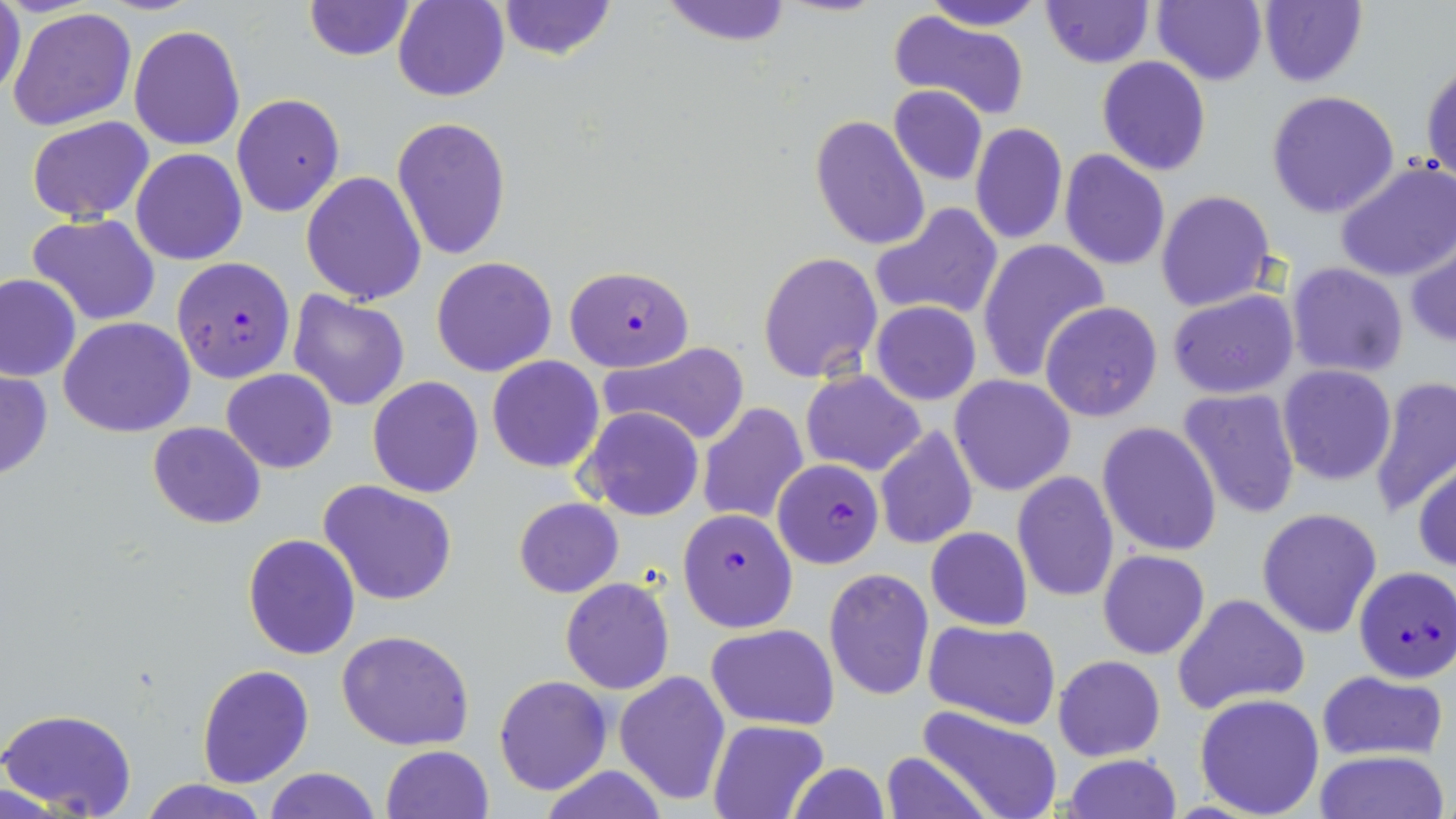

Approximate bounding boxes as (x1,y1)-(x2,y2) corner pairs in pixels. Uninfected red blood cell locations: (0,0)-(27,103), (303,0)-(416,60), (393,0)-(508,102), (492,0)-(619,63), (658,0)-(796,46), (920,0)-(1046,30), (1152,0)-(1267,85), (1260,0)-(1368,87), (1041,1)-(1155,68), (9,7)-(137,132), (888,11)-(1028,121), (130,24)-(246,151), (1421,54)-(1455,187), (1097,56)-(1211,176), (888,85)-(989,186), (1266,90)-(1400,218), (230,94)-(345,216), (809,114)-(929,252), (27,115)-(155,224), (392,116)-(512,261), (969,122)-(1068,246), (131,149)-(247,264), (1060,150)-(1170,272), (1335,161)-(1456,282), (300,171)-(426,305), (1155,190)-(1276,312), (871,203)-(1003,320), (29,212)-(161,325), (976,238)-(1110,384), (1406,243)-(1456,347), (758,251)-(883,384), (431,255)-(558,377), (1286,262)-(1408,379), (0,273)-(81,381), (1167,289)-(1299,400), (287,290)-(411,411), (871,301)-(981,405), (1040,301)-(1163,421), (59,316)-(196,438), (598,341)-(749,445), (487,356)-(606,472), (1278,365)-(1397,485), (0,367)-(52,483), (222,369)-(337,474), (800,370)-(926,476), (949,375)-(1077,496), (367,376)-(484,498), (1368,377)-(1456,522), (1177,387)-(1300,522), (697,402)-(809,525), (583,407)-(703,522), (147,421)-(266,529), (1097,422)-(1222,556), (874,425)-(978,550), (1414,460)-(1456,574), (1011,472)-(1118,602), (317,481)-(460,606), (513,497)-(623,599), (1257,507)-(1382,638), (925,526)-(1033,632), (242,534)-(361,660), (1098,550)-(1210,659), (823,567)-(934,702), (560,578)-(675,694), (1173,592)-(1311,714), (924,621)-(1060,730), (706,624)-(840,729), (337,630)-(476,751), (1053,653)-(1166,761), (197,662)-(313,788), (615,670)-(730,806), (1317,670)-(1449,763), (493,674)-(613,794), (1194,693)-(1326,818), (0,706)-(138,819), (915,706)-(1064,819), (707,719)-(830,819), (380,745)-(493,819), (879,750)-(992,819), (1311,750)-(1449,819), (1062,754)-(1181,818), (786,763)-(892,819), (535,764)-(671,819), (261,767)-(381,819), (135,778)-(270,819). Plasmodium falciparum-infected red blood cell locations: (171,257)-(295,382), (564,266)-(693,371), (774,459)-(885,569), (676,508)-(799,633), (1354,566)-(1456,683). Slide-level diagnosis: Plasmodium falciparum. May-Grünwald-Giemsa-stained preparation. Image is 1456×819 pixels. 1000x magnification. Thin blood film. Single field of view. Optical microscopy.